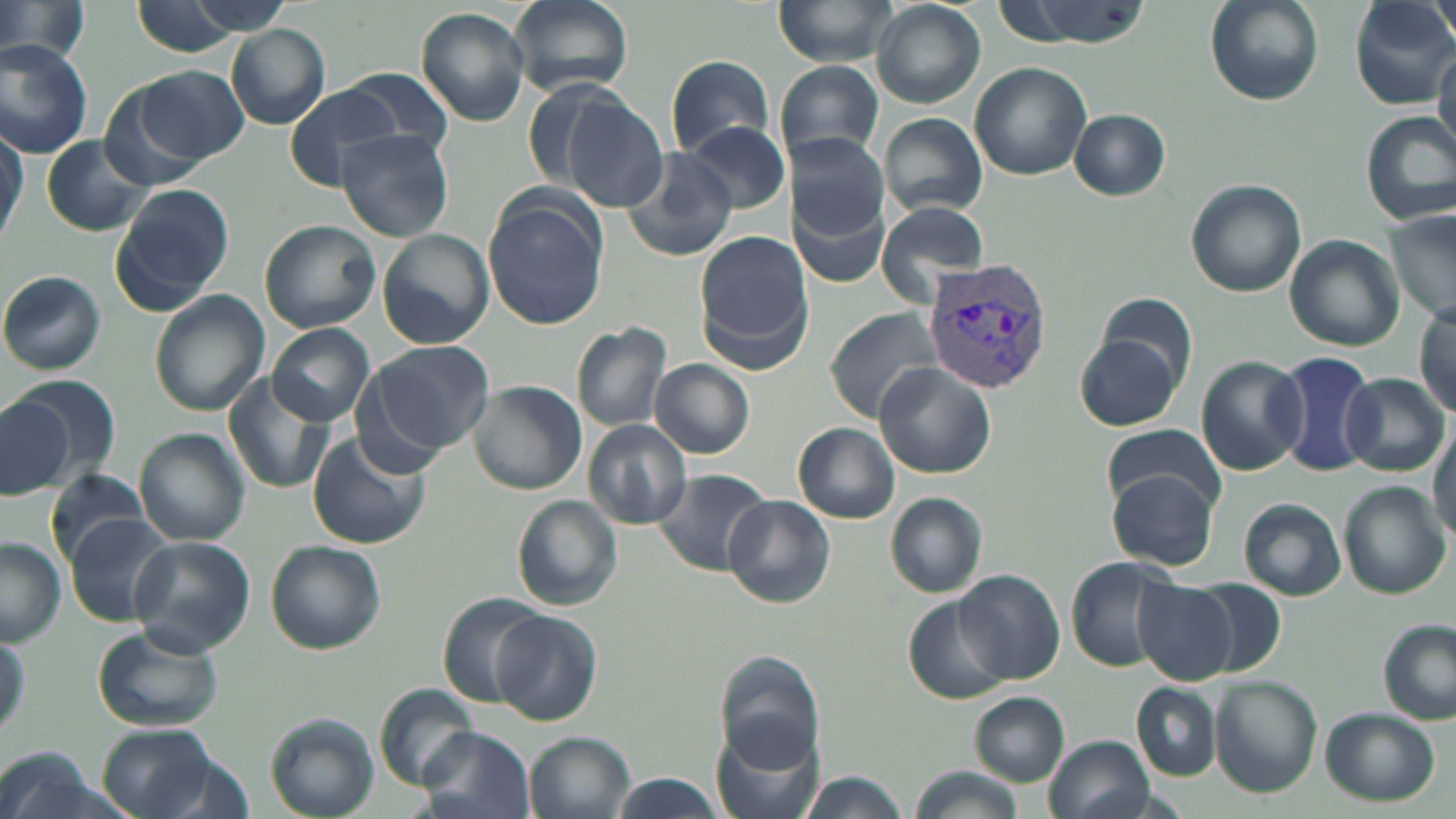 Approximate bounding boxes as (x1,y1)-(x2,y2) corner pairs in pixels. Uninfected red blood cell locations: (0,0)-(90,66), (508,0)-(633,96), (773,0)-(902,65), (995,0)-(1154,48), (1205,0)-(1323,105), (1350,0)-(1456,108), (1428,0)-(1456,43), (122,1)-(273,57), (872,2)-(985,108), (415,7)-(532,127), (226,23)-(330,129), (0,40)-(96,156), (1432,43)-(1456,154), (665,54)-(776,160), (775,60)-(885,164), (969,61)-(1092,179), (135,64)-(249,163), (339,68)-(453,153), (101,83)-(211,192), (283,84)-(405,190), (560,91)-(667,210), (1068,109)-(1170,200), (1361,111)-(1456,225), (879,113)-(988,217), (682,120)-(789,214), (334,128)-(454,242), (0,130)-(24,241), (789,131)-(889,238), (41,136)-(149,235), (619,148)-(739,261), (1184,180)-(1305,297), (792,183)-(891,289), (111,185)-(234,312), (482,190)-(611,334), (875,202)-(990,305), (1388,211)-(1455,326), (260,219)-(382,333), (377,229)-(495,350), (694,230)-(805,359), (1285,233)-(1403,352), (0,270)-(105,375), (147,291)-(268,416), (1091,293)-(1197,398), (1413,303)-(1455,415), (830,307)-(943,421), (571,321)-(672,433), (268,324)-(375,427), (1075,330)-(1183,431), (365,340)-(495,458), (1272,351)-(1380,476), (1195,355)-(1308,475), (649,359)-(756,459), (876,362)-(995,479), (5,372)-(118,485), (1340,372)-(1448,476), (222,373)-(335,492), (469,381)-(585,496), (0,395)-(73,499), (584,420)-(692,530), (792,422)-(900,523), (1103,423)-(1226,511), (1430,424)-(1456,547), (135,427)-(251,546), (309,431)-(431,548), (653,469)-(772,575), (1109,472)-(1219,570), (45,473)-(154,565), (1339,481)-(1451,598), (886,493)-(987,596), (510,494)-(623,613), (721,495)-(836,608), (1239,499)-(1347,602), (65,514)-(177,626), (129,535)-(254,654), (0,537)-(67,646), (266,540)-(386,654), (1065,557)-(1181,672), (954,569)-(1065,685), (1194,579)-(1289,676), (1131,580)-(1238,684), (437,593)-(546,705), (906,595)-(1013,704), (492,610)-(603,727), (1379,620)-(1455,725), (92,625)-(225,732), (0,634)-(28,742), (714,653)-(824,768), (1209,676)-(1322,796), (1132,683)-(1221,779), (374,685)-(481,793), (971,691)-(1070,788), (1318,707)-(1440,806), (264,714)-(377,818), (97,724)-(223,818), (712,724)-(825,819), (417,727)-(535,819), (527,732)-(636,819), (1047,734)-(1151,819), (1,746)-(96,819), (133,752)-(257,819), (910,765)-(1023,819), (794,771)-(911,819), (609,775)-(726,819). Plasmodium vivax-infected red blood cell locations: (921,257)-(1056,392). Slide-level diagnosis: Plasmodium vivax. Thin blood smear. Single field of view. Image is 1456×819 pixels. 1000x magnification. Light microscopy. May-Grünwald-Giemsa stain.